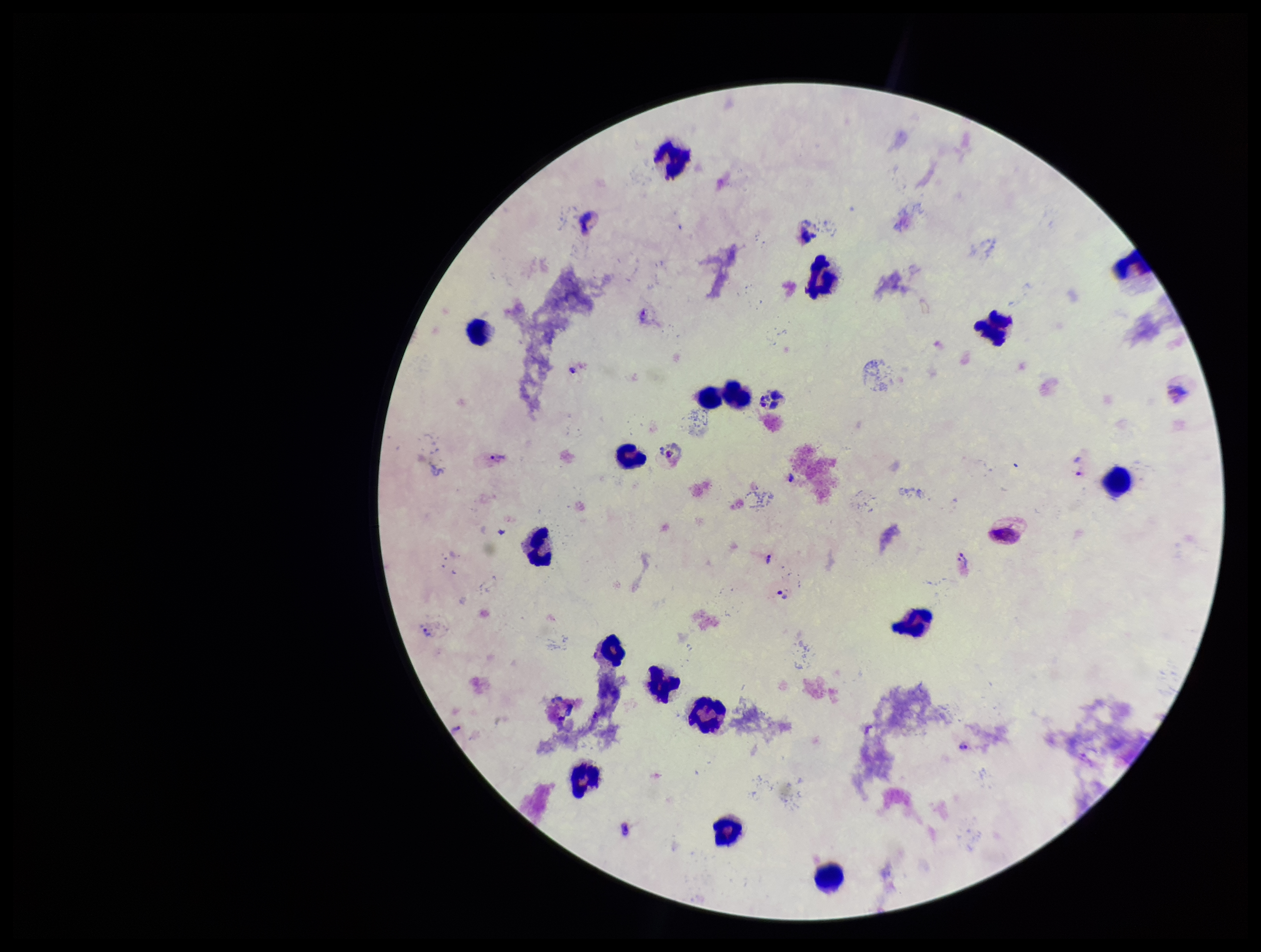

Smartphone photograph taken through the eyepiece of a microscope. Plasmodium parasites: identified. Preparation: thick smear. Parasite count: 4. Leukocyte count: 17. Image is 1261×952 pixels. Giemsa stain. Patient malaria status: infected. Species reported for this patient: Plasmodium vivax. One field from this slide.